Give the extent of all Plasmodium malariae-infected red blood cells.
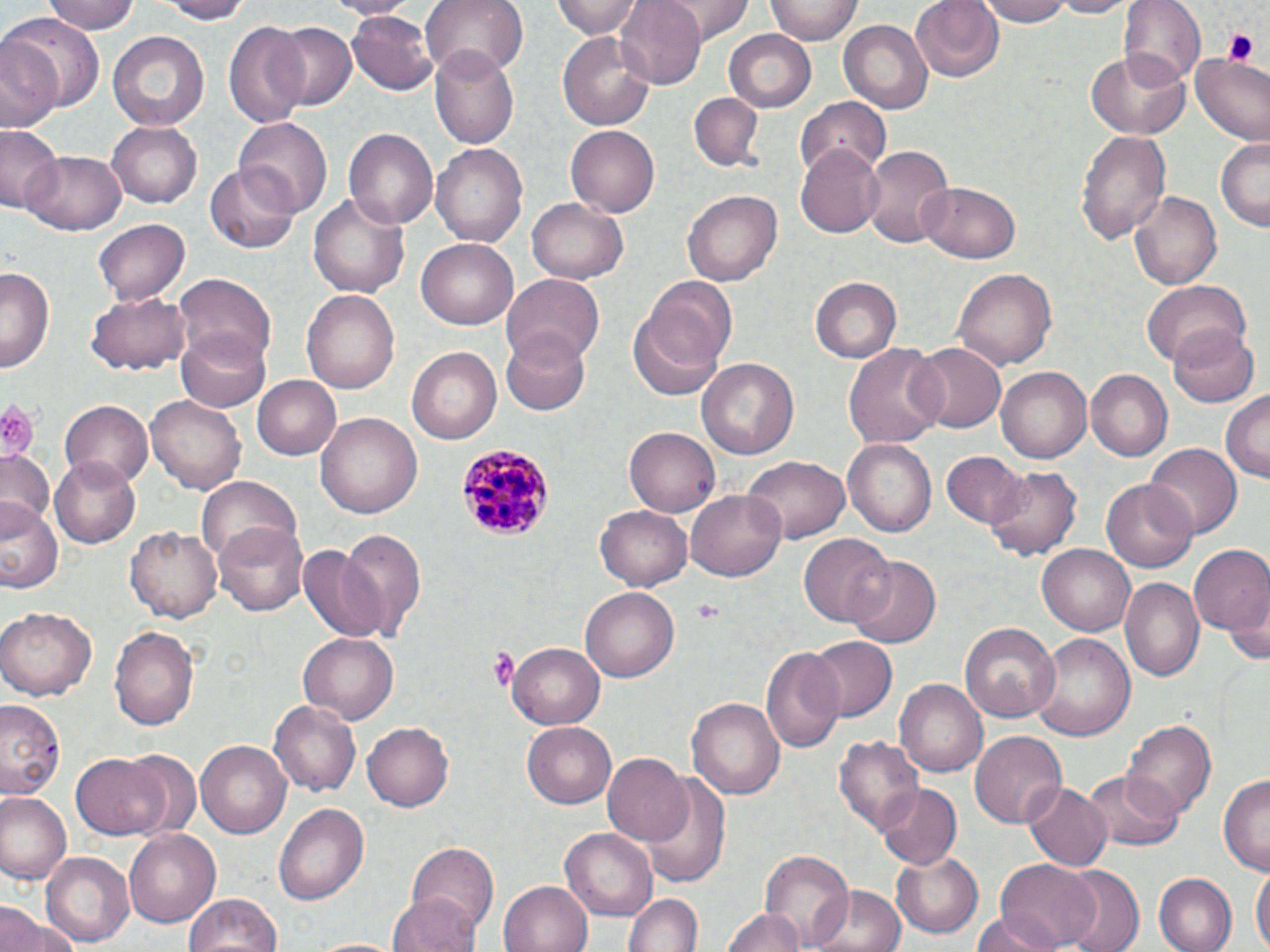
Approximate bounding boxes as (x1, y1, x2, y2) in pixels.
Plasmodium malariae-infected red blood cells: (455, 442, 557, 544).

Summary:
  - Uninfected red blood cell locations: (46, 0, 138, 35), (157, 0, 249, 23), (323, 0, 418, 18), (419, 0, 526, 82), (553, 0, 645, 37), (614, 0, 706, 87), (659, 0, 754, 41), (766, 0, 863, 44), (910, 0, 1005, 84), (976, 0, 1077, 26), (1050, 0, 1132, 17), (1121, 0, 1205, 87), (348, 11, 438, 95), (3, 12, 106, 112), (223, 17, 312, 133), (837, 19, 933, 113), (268, 20, 356, 113), (106, 30, 211, 131), (723, 30, 817, 112), (557, 31, 656, 131), (0, 35, 62, 134), (430, 46, 522, 148), (1084, 51, 1189, 139), (1188, 51, 1270, 143), (689, 92, 764, 170), (796, 97, 892, 178), (234, 118, 333, 216), (108, 121, 202, 208), (0, 122, 64, 215), (565, 126, 659, 218), (341, 128, 437, 229), (1077, 129, 1170, 247), (1215, 136, 1269, 232), (432, 142, 528, 246), (862, 143, 954, 247), (796, 147, 885, 237), (22, 151, 125, 235), (205, 165, 300, 252), (920, 181, 1022, 262), (308, 190, 411, 300), (682, 190, 784, 286), (1130, 190, 1223, 290), (527, 198, 630, 284), (93, 218, 191, 304), (417, 237, 519, 330), (1, 265, 56, 371), (954, 267, 1058, 370), (503, 273, 606, 368), (172, 274, 276, 367), (643, 276, 738, 375), (811, 276, 901, 361), (1139, 280, 1255, 367), (302, 288, 400, 394), (87, 293, 189, 374), (629, 308, 726, 401), (1169, 325, 1260, 406), (176, 328, 272, 411), (501, 329, 591, 415), (842, 340, 944, 449), (910, 342, 1007, 434), (407, 346, 501, 444), (699, 356, 799, 461), (996, 365, 1093, 464), (1086, 370, 1172, 460), (251, 375, 341, 462), (146, 391, 248, 492), (1220, 391, 1269, 482), (59, 399, 150, 485), (318, 412, 422, 518), (625, 427, 720, 515), (844, 438, 940, 538), (1145, 443, 1242, 538), (0, 448, 56, 531), (942, 451, 1024, 530), (740, 455, 850, 543), (50, 456, 145, 548), (985, 465, 1081, 559), (195, 477, 299, 568), (1101, 479, 1197, 573), (687, 489, 788, 581), (1, 502, 62, 596), (595, 505, 692, 591), (126, 521, 224, 623), (214, 521, 309, 615), (338, 526, 427, 640), (801, 535, 894, 626), (1037, 544, 1135, 635), (298, 545, 389, 645), (1188, 546, 1270, 638), (848, 555, 940, 649), (1121, 576, 1203, 683), (580, 584, 678, 679), (1226, 585, 1270, 668), (0, 605, 98, 700), (960, 620, 1061, 723), (109, 626, 200, 731), (1030, 633, 1135, 742), (297, 634, 400, 722), (806, 635, 898, 723), (509, 640, 608, 730), (763, 646, 845, 754), (897, 679, 987, 778), (686, 694, 785, 797), (0, 700, 67, 801), (269, 701, 361, 795), (1122, 718, 1215, 824), (521, 720, 619, 809), (363, 722, 455, 811), (969, 731, 1067, 829), (835, 736, 924, 837), (197, 740, 291, 838), (123, 749, 200, 837), (72, 753, 167, 838), (601, 753, 694, 847), (1083, 769, 1183, 853), (644, 771, 730, 889), (1220, 775, 1270, 873), (874, 782, 961, 869), (1023, 782, 1112, 874), (0, 792, 69, 882), (274, 802, 369, 906), (559, 827, 657, 917), (123, 829, 223, 928), (407, 842, 498, 932), (759, 848, 855, 950), (42, 851, 135, 948), (892, 854, 984, 938), (994, 861, 1099, 949), (1252, 865, 1269, 952), (1058, 868, 1143, 952), (1153, 874, 1236, 952), (500, 880, 593, 952), (808, 884, 906, 952), (624, 890, 703, 952), (183, 891, 283, 952), (388, 892, 481, 952), (1, 903, 38, 952), (2, 907, 80, 952), (722, 907, 805, 952), (974, 915, 1058, 952)
  - Platelet locations: (1222, 29, 1260, 66), (0, 400, 42, 462), (692, 600, 719, 619), (486, 646, 520, 690)
  - Slide-level diagnosis: Plasmodium malariae
  - Preparation: thin blood film
  - Field of view: one of a larger specimen
  - Magnification: 1000x
  - Modality: light microscopy
  - Stain: May-Grünwald-Giemsa
  - Image size: 1270×952 pixels